Outline each blood parasite and name the species.
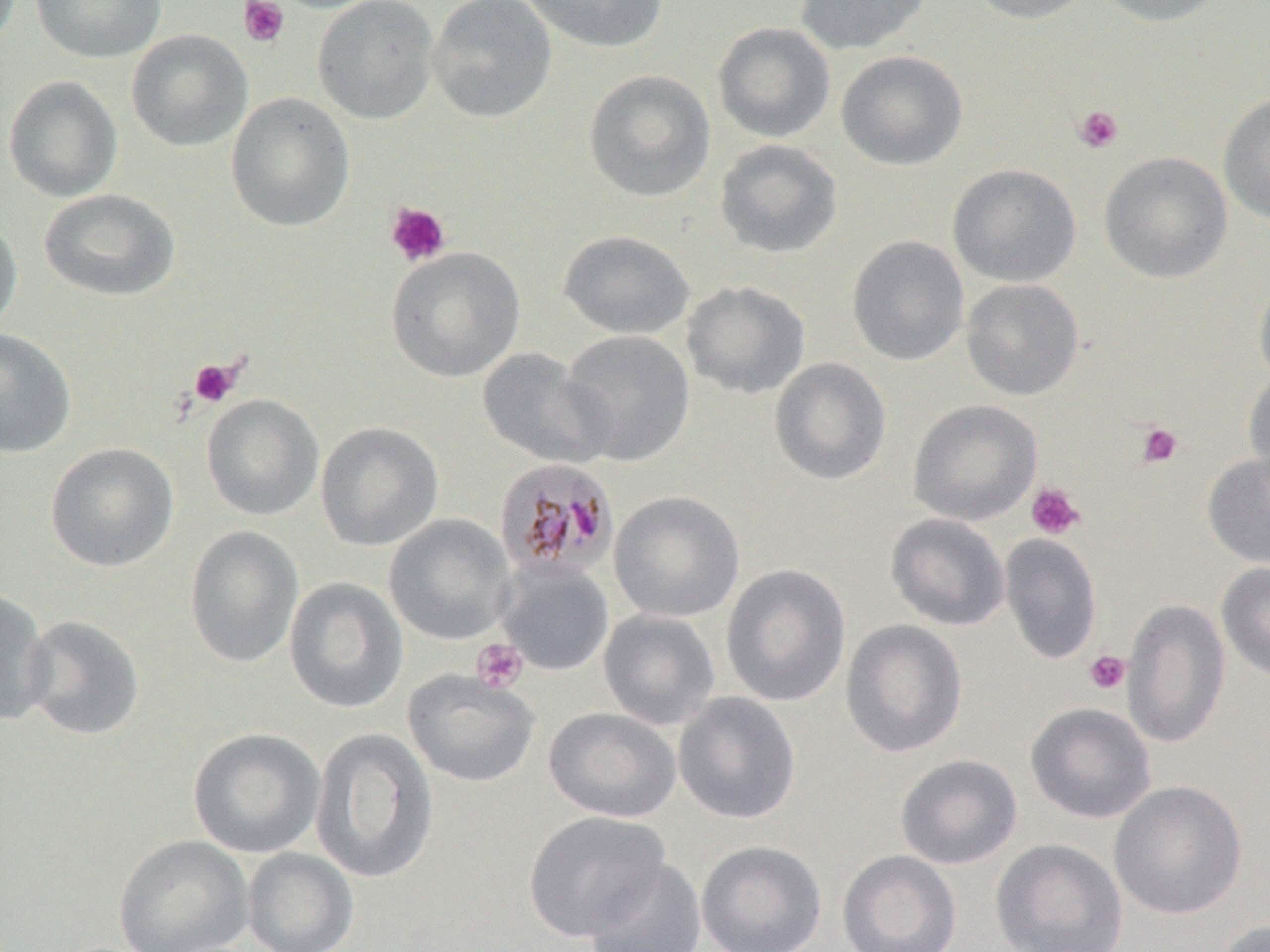

Approximate bounding boxes as named x1/y1/x2/y2 corners in pixels.
Plasmodium malariae-infected red blood cells: (x1=494, y1=457, x2=620, y2=582).
No Plasmodium falciparum, Plasmodium ovale, Plasmodium vivax, Babesia divergens, or Trypanosoma brucei observed.

slide-level diagnosis = Plasmodium malariae
image size = 1270×952 pixels
modality = light microscopy
uninfected red blood cell locations = approximate bounding boxes as named x1/y1/x2/y2 corners in pixels: (x1=31, y1=0, x2=166, y2=64), (x1=312, y1=0, x2=440, y2=124), (x1=426, y1=0, x2=557, y2=123), (x1=517, y1=0, x2=670, y2=53), (x1=794, y1=0, x2=931, y2=55), (x1=966, y1=0, x2=1099, y2=23), (x1=1095, y1=0, x2=1230, y2=27), (x1=712, y1=21, x2=836, y2=143), (x1=126, y1=30, x2=253, y2=152), (x1=836, y1=49, x2=968, y2=171), (x1=583, y1=69, x2=716, y2=202), (x1=2, y1=75, x2=123, y2=203), (x1=225, y1=92, x2=355, y2=232), (x1=1218, y1=93, x2=1270, y2=225), (x1=714, y1=139, x2=843, y2=259), (x1=1099, y1=151, x2=1232, y2=283), (x1=947, y1=163, x2=1081, y2=287), (x1=38, y1=189, x2=181, y2=302), (x1=0, y1=213, x2=22, y2=336), (x1=558, y1=229, x2=695, y2=340), (x1=847, y1=235, x2=969, y2=366), (x1=385, y1=246, x2=525, y2=383), (x1=1254, y1=272, x2=1270, y2=389), (x1=961, y1=279, x2=1084, y2=400), (x1=681, y1=280, x2=811, y2=399), (x1=0, y1=328, x2=77, y2=459), (x1=559, y1=330, x2=696, y2=467), (x1=477, y1=347, x2=611, y2=470), (x1=769, y1=357, x2=892, y2=486), (x1=1243, y1=368, x2=1270, y2=488), (x1=201, y1=394, x2=323, y2=521), (x1=907, y1=399, x2=1043, y2=526), (x1=315, y1=421, x2=443, y2=551), (x1=44, y1=442, x2=179, y2=572), (x1=1202, y1=452, x2=1270, y2=569), (x1=609, y1=491, x2=745, y2=623), (x1=885, y1=513, x2=1010, y2=631), (x1=383, y1=514, x2=517, y2=645), (x1=183, y1=526, x2=303, y2=669), (x1=999, y1=532, x2=1102, y2=665), (x1=495, y1=560, x2=614, y2=676), (x1=1217, y1=561, x2=1270, y2=683), (x1=721, y1=563, x2=851, y2=707), (x1=284, y1=577, x2=409, y2=714), (x1=0, y1=588, x2=55, y2=727), (x1=1123, y1=599, x2=1230, y2=748), (x1=598, y1=609, x2=720, y2=730), (x1=22, y1=615, x2=145, y2=740), (x1=840, y1=619, x2=968, y2=758), (x1=403, y1=669, x2=540, y2=788), (x1=673, y1=692, x2=801, y2=825), (x1=1025, y1=702, x2=1156, y2=824), (x1=543, y1=707, x2=681, y2=822), (x1=187, y1=727, x2=326, y2=858), (x1=310, y1=727, x2=439, y2=883), (x1=896, y1=754, x2=1022, y2=869), (x1=1109, y1=781, x2=1247, y2=920), (x1=522, y1=810, x2=670, y2=942), (x1=113, y1=834, x2=255, y2=952), (x1=990, y1=838, x2=1128, y2=951), (x1=696, y1=840, x2=827, y2=952), (x1=242, y1=848, x2=359, y2=952), (x1=838, y1=850, x2=962, y2=952), (x1=583, y1=857, x2=707, y2=951), (x1=1214, y1=919, x2=1270, y2=952)
preparation = thin blood smear
platelet locations = approximate bounding boxes as named x1/y1/x2/y2 corners in pixels: (x1=238, y1=0, x2=289, y2=48), (x1=1073, y1=105, x2=1123, y2=153), (x1=386, y1=202, x2=451, y2=267), (x1=188, y1=357, x2=243, y2=408), (x1=1135, y1=422, x2=1183, y2=468), (x1=1026, y1=481, x2=1086, y2=540), (x1=471, y1=638, x2=528, y2=694), (x1=1084, y1=650, x2=1130, y2=695)
magnification = 1000x
stain = May-Grünwald-Giemsa
field of view = one of a larger specimen